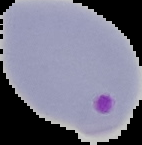
{
  "image_type": "cell region segmented out of the field of view; surrounding area masked to black",
  "image_size": "142×145 pixels",
  "result": "malaria parasites detected",
  "preparation": "thin blood smear"
}